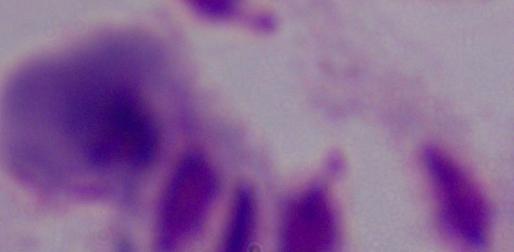

Summary:
  - Magnification: 1000x
  - Modality: micrograph
  - Identification: trichomonad